Name the cell type shown.
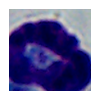

This is a leukocyte.

Summary:
  - Modality: micrograph
  - Magnification: 1000x